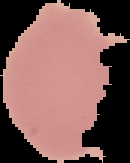
Summary:
  - Result: negative for malaria parasites
  - Image size: 130×163 pixels
  - Image type: cell region segmented out of the field of view; surrounding area masked to black
  - Preparation: thin blood smear